Classify this cell by malaria status.
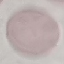

It is uninfected.

preparation: thin smear
stain: Giemsa
image_type: cell patch, automatically extracted from a larger field of view and resized to 64 × 64 pixels
capture: smartphone through the microscope eyepiece